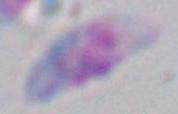
Toxoplasma gondii is seen. 1000x magnification. Photomicrograph.